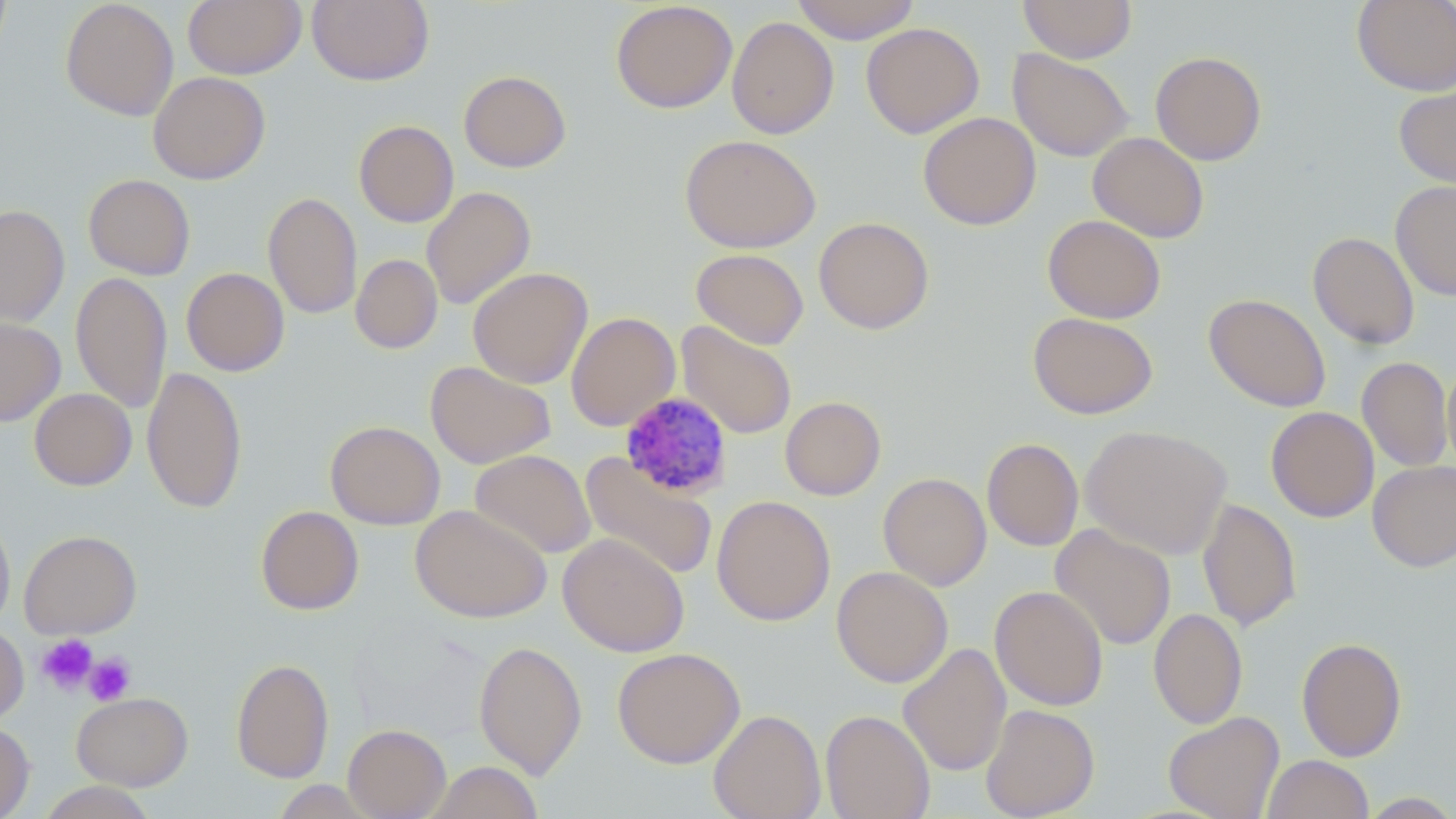

slide-level diagnosis = Plasmodium malariae
image size = 1456×819 pixels
Plasmodium malariae-infected red blood cell locations = approximate bounding boxes as (x1, y1, x2, y2) in pixels: (619, 391, 734, 501)
platelet locations = approximate bounding boxes as (x1, y1, x2, y2) in pixels: (36, 634, 98, 694), (83, 652, 137, 706)
stain = May-Grünwald-Giemsa
uninfected red blood cell locations = approximate bounding boxes as (x1, y1, x2, y2) in pixels: (0, 0, 11, 61), (60, 0, 179, 121), (183, 0, 306, 79), (307, 0, 435, 87), (790, 0, 921, 44), (1017, 0, 1138, 63), (1352, 0, 1456, 96), (610, 1, 737, 114), (727, 16, 839, 139), (861, 22, 985, 139), (1008, 48, 1134, 162), (1150, 51, 1267, 166), (458, 70, 571, 173), (148, 71, 271, 185), (1394, 81, 1456, 190), (918, 112, 1042, 231), (353, 120, 459, 227), (1088, 132, 1209, 243), (680, 134, 820, 253), (83, 174, 195, 280), (1390, 180, 1456, 301), (422, 186, 536, 310), (263, 192, 362, 319), (0, 204, 70, 328), (1042, 214, 1166, 323), (813, 216, 934, 334), (1308, 231, 1420, 350), (692, 248, 809, 350), (351, 254, 443, 354), (468, 267, 593, 388), (181, 268, 290, 376), (71, 271, 172, 414), (1204, 293, 1331, 412), (566, 312, 680, 431), (1028, 312, 1158, 420), (0, 317, 65, 426), (676, 321, 797, 439), (1357, 356, 1453, 471), (425, 361, 556, 469), (1442, 361, 1456, 473), (142, 366, 246, 514), (29, 388, 137, 490), (780, 396, 886, 501), (1266, 406, 1378, 523), (325, 420, 445, 530), (1081, 424, 1233, 559), (982, 438, 1083, 551), (469, 450, 596, 559), (579, 452, 718, 582), (1367, 460, 1456, 572), (878, 472, 992, 591), (711, 495, 835, 626), (1197, 498, 1301, 632), (410, 504, 552, 623), (255, 506, 364, 615), (0, 508, 15, 635), (1051, 524, 1176, 651), (19, 530, 142, 638), (558, 533, 689, 657), (831, 566, 953, 688), (989, 585, 1108, 711), (1149, 608, 1247, 729), (0, 624, 29, 725), (1296, 637, 1407, 761), (474, 640, 588, 779), (898, 643, 1011, 776), (612, 647, 745, 768), (230, 658, 334, 783), (72, 692, 193, 790), (980, 703, 1100, 819), (708, 709, 826, 819), (820, 709, 935, 819), (1163, 711, 1285, 819), (0, 720, 35, 819), (343, 724, 451, 819), (1262, 754, 1374, 818), (426, 761, 543, 819), (271, 780, 378, 818), (34, 782, 160, 819), (1357, 792, 1456, 818)
field of view = one of a larger specimen
modality = light microscopy
preparation = thin blood smear
magnification = 1000x